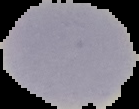
Summary:
  - Image type: cell region segmented out of the field of view; surrounding area masked to black
  - Preparation: thin blood film
  - Image size: 139×109 pixels
  - Result: negative for malaria parasites